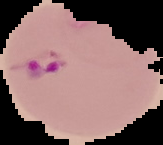
malaria status = parasitized
image type = segmented cell region on a black background
image size = 163×145 pixels
preparation = thin blood film